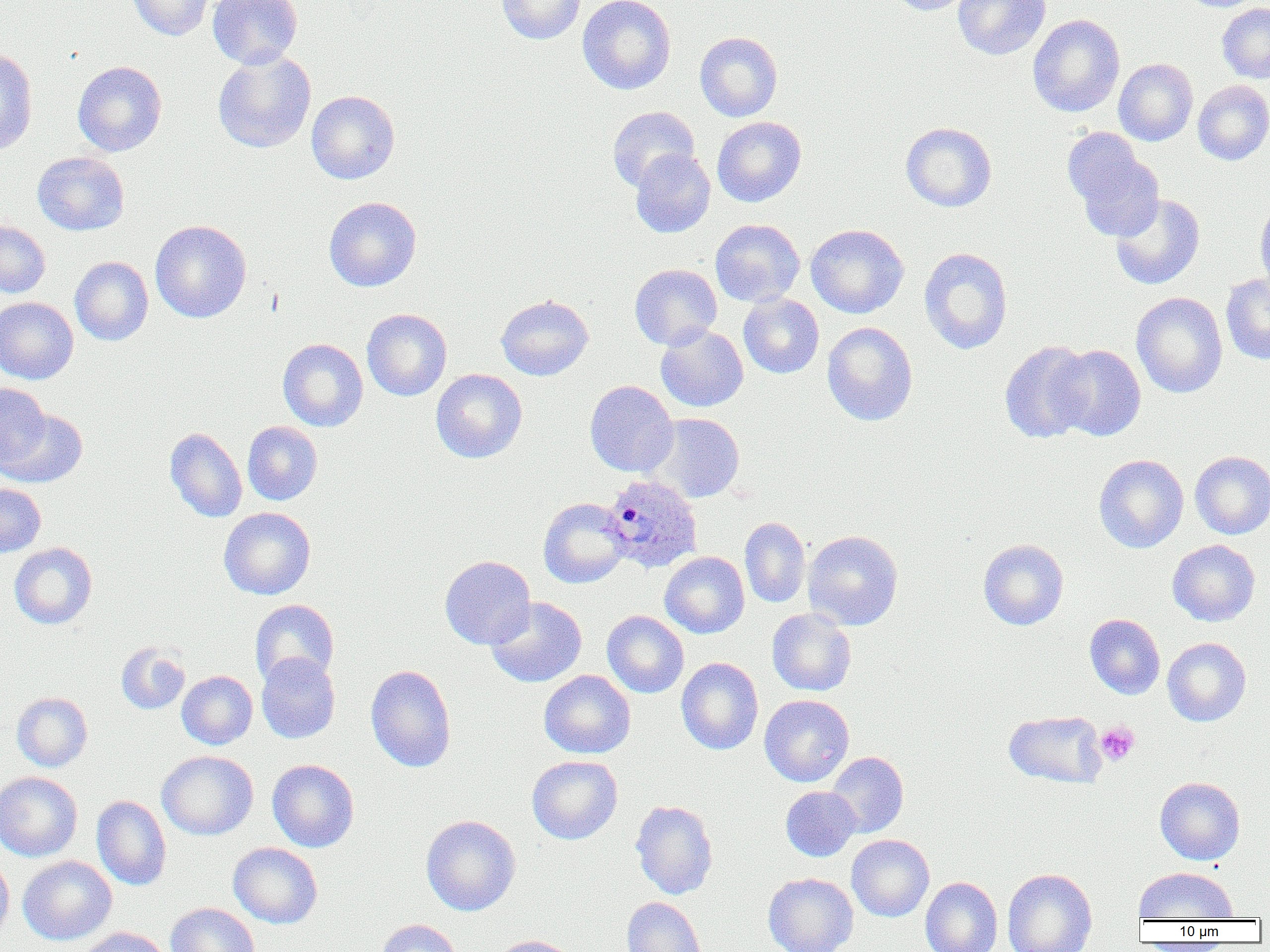
{
  "plasmodium_ovale_infected_red_blood_cell_locations": "approximate bounding boxes as (x1,y1)-(x2,y2) corner pairs in pixels: (602,473)-(703,573)",
  "slide_level_diagnosis": "Plasmodium ovale",
  "image_size": "1270×952 pixels",
  "preparation": "thin blood smear",
  "modality": "optical microscopy",
  "platelet_locations": "approximate bounding boxes as (x1,y1)-(x2,y2) corner pairs in pixels: (1095,722)-(1139,766)",
  "uninfected_red_blood_cell_locations": "approximate bounding boxes as (x1,y1)-(x2,y2) corner pairs in pixels: (127,0)-(215,40), (208,0)-(302,69), (496,0)-(585,44), (577,0)-(676,94), (889,0)-(976,16), (953,0)-(1051,60), (1217,4)-(1270,83), (1027,15)-(1125,117), (694,32)-(783,121), (0,47)-(38,156), (212,50)-(316,154), (1113,58)-(1198,146), (73,61)-(167,156), (1193,80)-(1270,165), (306,90)-(400,184), (607,106)-(700,191), (712,116)-(806,207), (900,122)-(997,212), (1064,131)-(1163,240), (630,149)-(716,238), (32,152)-(129,235), (1109,193)-(1206,291), (324,197)-(422,291), (1255,199)-(1270,299), (0,219)-(50,298), (710,219)-(805,307), (150,220)-(251,323), (805,224)-(909,318), (919,247)-(1013,355), (70,257)-(153,346), (630,264)-(722,350), (1220,273)-(1270,364), (1131,292)-(1228,398), (495,294)-(594,381), (738,294)-(824,378), (0,297)-(78,384), (362,309)-(452,401), (822,322)-(917,426), (655,325)-(748,412), (278,338)-(368,432), (1000,340)-(1095,444), (1050,345)-(1146,441), (430,369)-(527,463), (584,380)-(678,477), (1,382)-(50,469), (2,408)-(89,488), (648,412)-(745,503), (242,421)-(323,505), (165,427)-(247,522), (1190,451)-(1270,539), (1093,454)-(1189,553), (0,483)-(46,556), (538,497)-(630,588), (218,507)-(316,599), (739,517)-(810,608), (803,530)-(903,629), (978,539)-(1069,630), (1167,539)-(1260,626), (9,543)-(97,629), (660,551)-(749,638), (440,555)-(535,649), (486,596)-(587,688), (250,599)-(339,686), (767,609)-(856,696), (602,610)-(689,698), (1084,613)-(1165,699), (1162,638)-(1251,726), (116,642)-(190,714), (256,653)-(340,743), (676,657)-(763,755), (366,665)-(456,772), (539,670)-(635,758), (177,671)-(257,749), (11,692)-(92,771), (759,695)-(854,787), (1003,710)-(1107,789), (157,750)-(258,840), (826,751)-(909,838), (526,755)-(622,844), (267,759)-(359,852), (0,770)-(82,862), (1155,776)-(1245,865), (781,786)-(860,861), (92,795)-(171,890), (630,800)-(718,900), (421,814)-(521,915), (847,834)-(934,921), (228,843)-(323,929), (0,854)-(14,942), (18,856)-(116,944), (1133,866)-(1238,921), (1002,868)-(1097,952), (763,873)-(858,952), (920,877)-(1003,952), (622,897)-(706,952), (165,902)-(259,952), (376,919)-(462,952), (77,926)-(169,952), (490,935)-(582,952)",
  "field_of_view": "single",
  "magnification": "1000x"
}